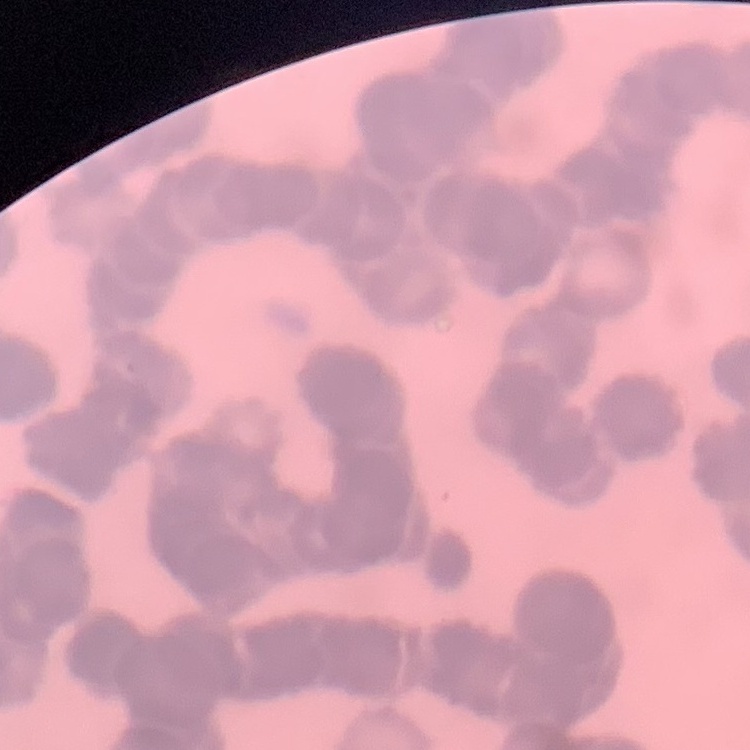

The red blood cells show rouleaux formation. Thin peripheral smear. Square crop of a larger photomicrograph. Stained with either Field's or Giemsa.